Report the malaria status of this cell.
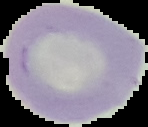
Uninfected.

Summary:
  - Image type: segmented cell region with the area outside set to black
  - Preparation: thin blood film
  - Image size: 148×127 pixels